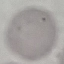

malaria status = uninfected
stain = Giemsa
capture = smartphone through the microscope eyepiece
image type = cell patch, automatically extracted from a larger field of view and resized to 64 × 64 pixels
preparation = thin smear